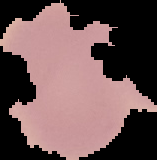
Summary:
  - Image type: segmented cell region on a black background
  - Preparation: thin blood smear
  - Result: no Plasmodium parasites detected
  - Image size: 157×160 pixels